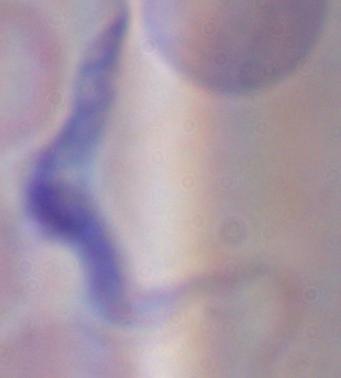

Summary:
  - Modality: photomicrograph
  - Identification: trypanosome
  - Magnification: 1000x